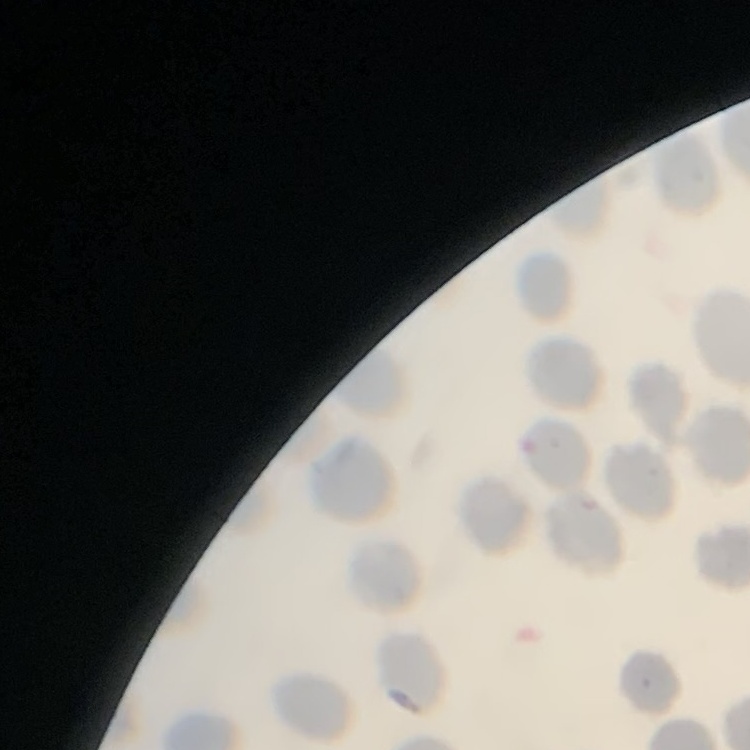
The erythrocytes exhibit no rouleaux formation. Thin blood film. Stained with either Field's or Giemsa. Square crop of a larger photomicrograph.